Assess this cell for malaria.
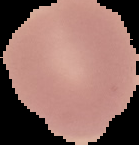

Uninfected.

Summary:
  - Preparation: thin blood film
  - Image size: 139×145 pixels
  - Image type: cell region segmented out of the field of view; surrounding area masked to black